Locate every malaria parasite.
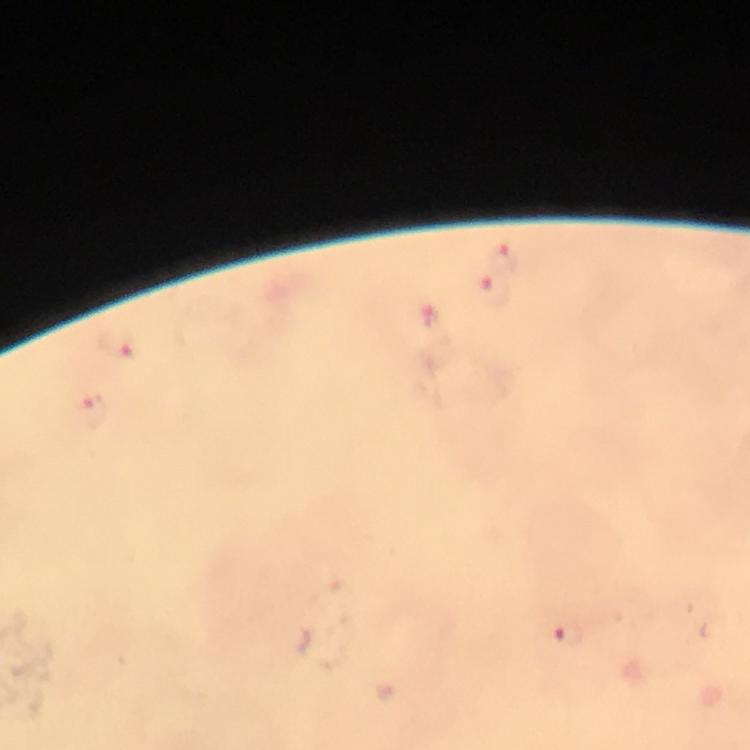

Approximate centers as (x, y) in pixels.
Malaria parasites: (501, 256), (493, 292), (431, 314), (119, 346), (92, 412), (568, 635).

Summary:
  - Stain: Giemsa
  - Context: from a malaria diagnostic workup
  - Cropped from: one field of view
  - Capture: smartphone mounted on the microscope
  - Preparation: thick smear
  - Magnification: 100x
  - Immersion oil: applied
  - Image size: 750×750 pixels